Evaluate for malaria.
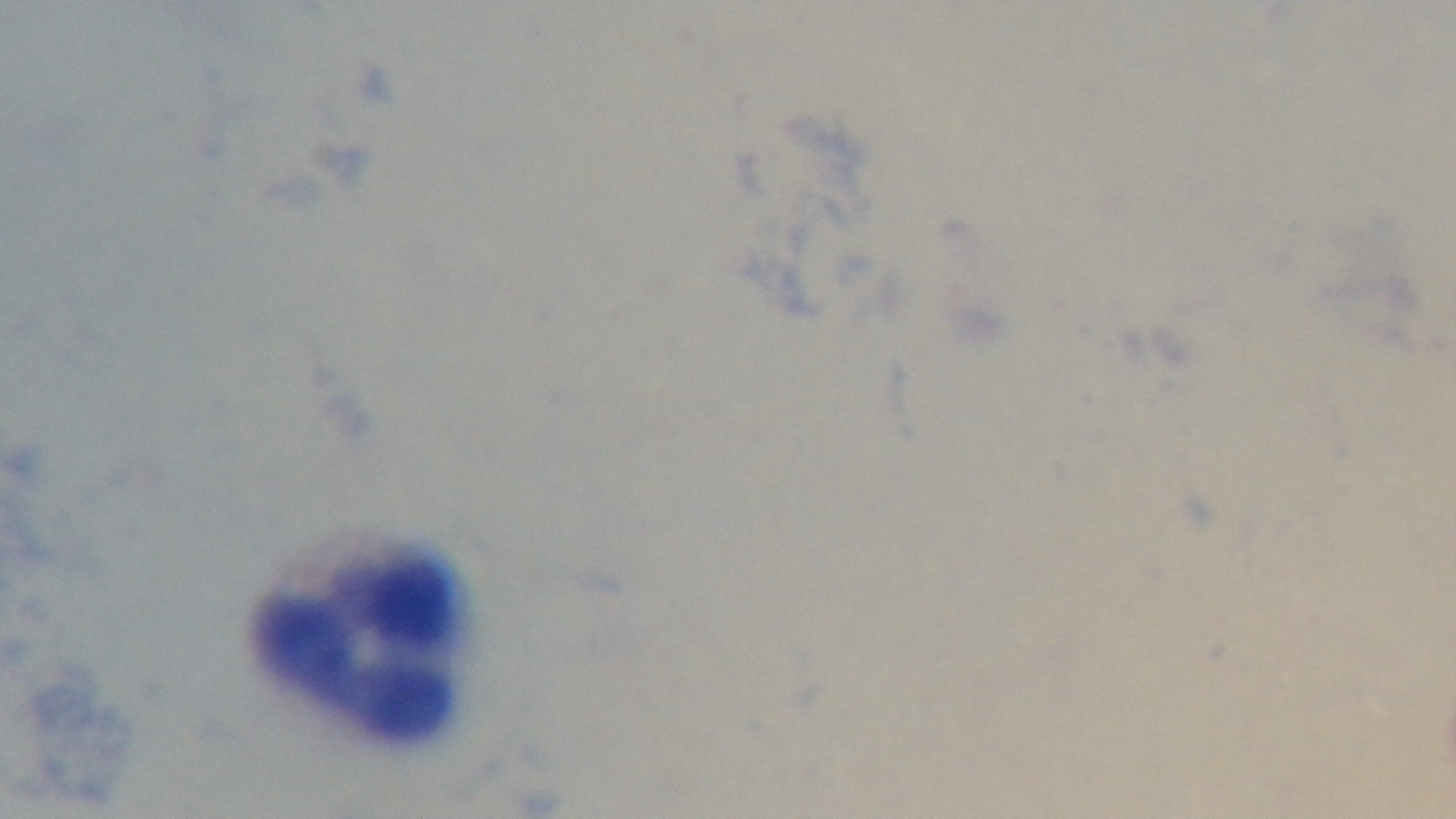

Negative.

Photomicrograph. Preparation: thick. 100x oil-immersion objective. One field from the slide. Giemsa stain. Captured with a mounted 4K digital camera.